Assess this cell for malaria.
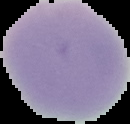

It is uninfected.

Summary:
  - Image size: 130×124 pixels
  - Image type: segmented cell region with the area outside set to black
  - Preparation: thin blood film